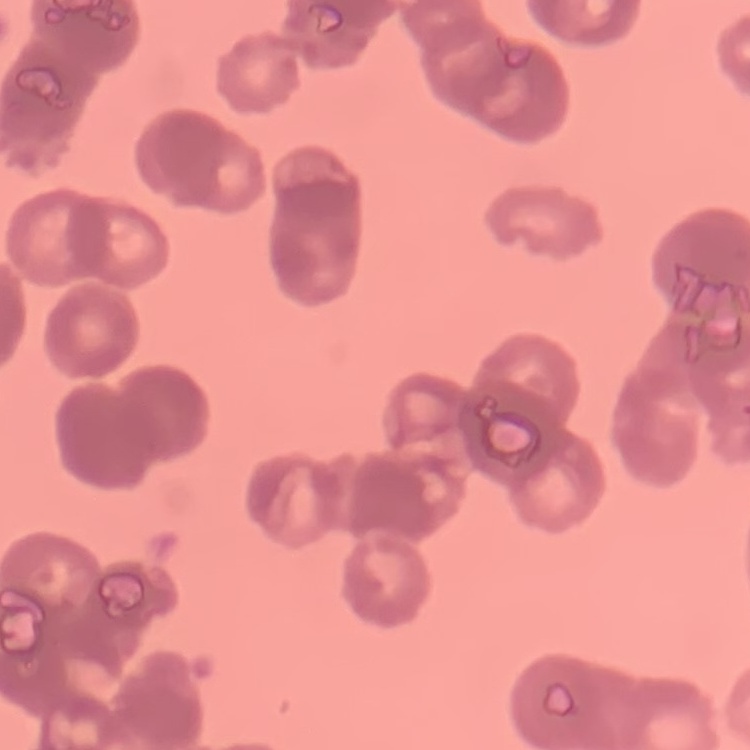
The red blood cells exhibit rouleaux formation. Square crop of a larger photomicrograph. Stained with either Field's or Giemsa. Thin peripheral smear.